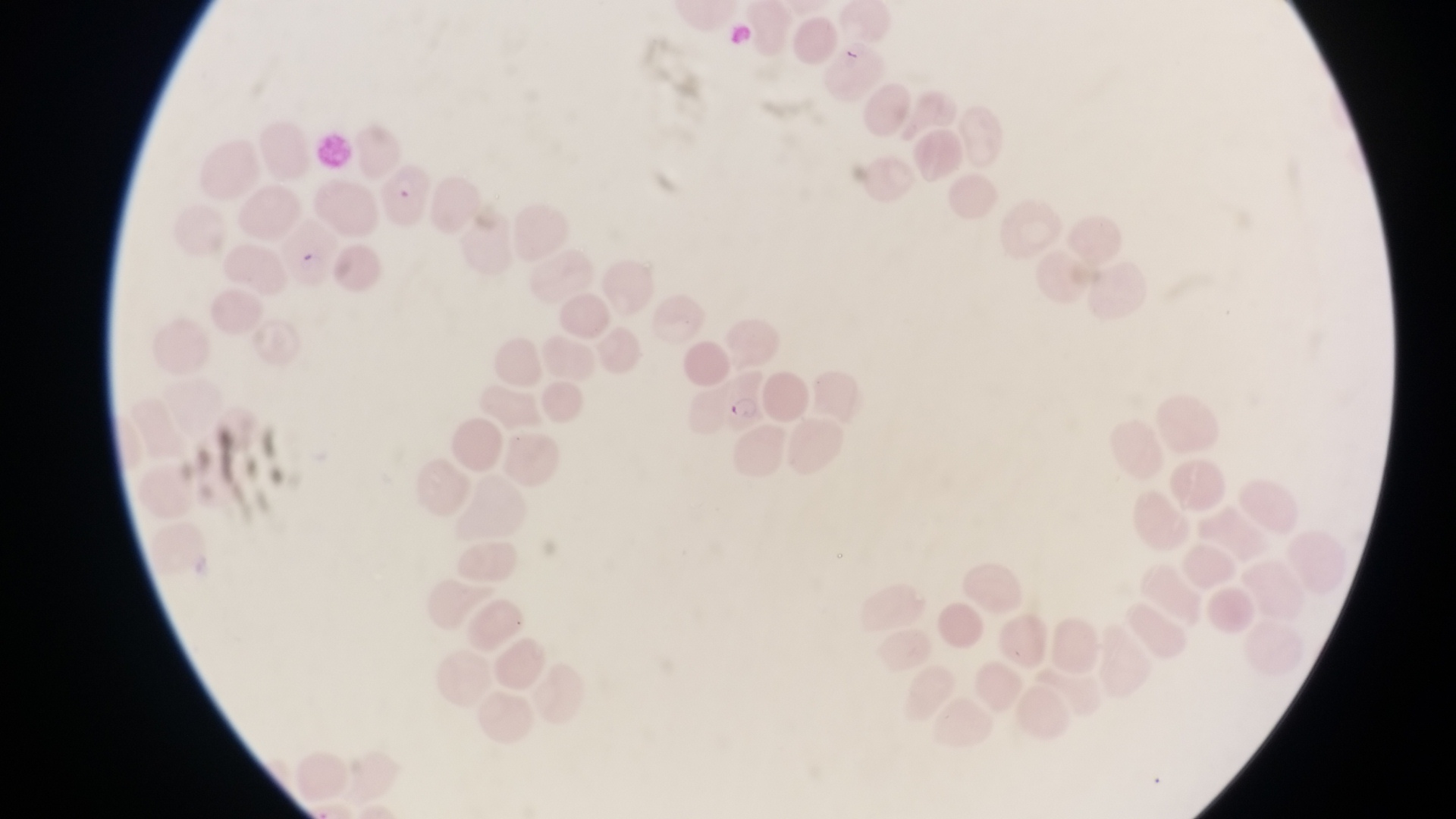

Approximate bounding boxes as left top right bottom in pixels.
Summary:
  - Parasitised red blood cell locations: 381 159 430 230; 716 367 769 434
  - Artifact (platelet-like body, stain precipitate, or debris) locations: 296 249 322 275
  - Magnification: 1000x
  - Capture: smartphone photograph through the eyepiece of an Olympus CX-23 microscope
  - Preparation: thin blood smear
  - Image size: 1456×819 pixels
  - Country: Uganda
  - Field of view: single